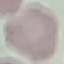
Summary:
  - Malaria status: uninfected
  - Stain: Giemsa
  - Preparation: thin blood film
  - Capture: smartphone camera at the microscope eyepiece
  - Image type: cell patch, automatically extracted from a larger field of view and resized to 64 × 64 pixels